State the blood parasite species.
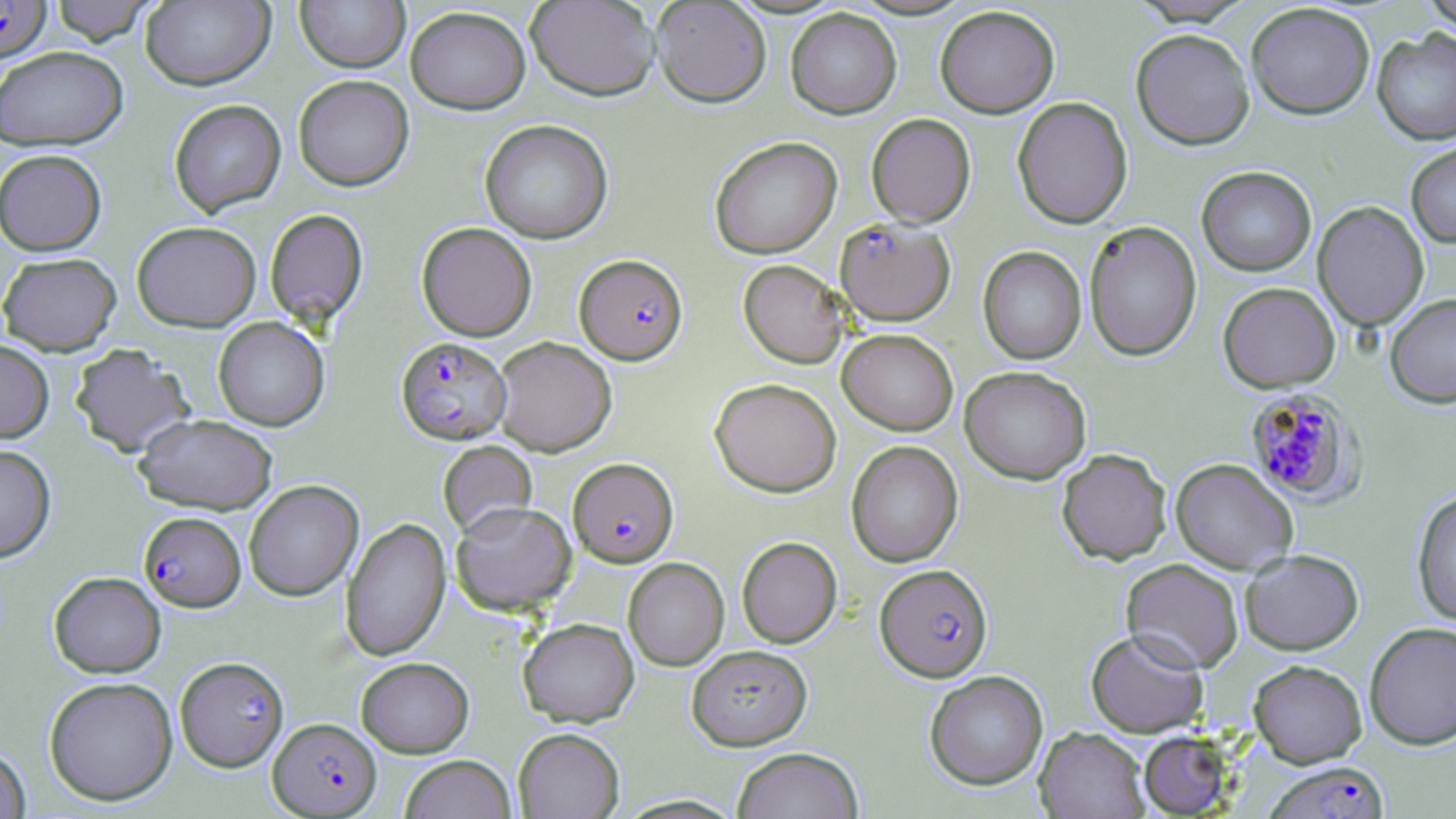
Plasmodium falciparum.

Approximate bounding boxes as (x1,y1)-(x2,y2) corner pairs in pixels. Uninfected red blood cell locations: (46,0)-(161,45), (295,0)-(410,73), (525,0)-(660,101), (1419,0)-(1456,35), (140,1)-(275,90), (651,1)-(771,107), (1245,2)-(1375,119), (405,5)-(530,114), (934,5)-(1059,118), (785,8)-(902,119), (1131,28)-(1255,150), (1372,29)-(1456,146), (0,46)-(128,151), (293,74)-(414,191), (1012,96)-(1133,228), (168,99)-(286,217), (866,113)-(976,228), (479,119)-(613,244), (709,136)-(842,259), (1406,141)-(1456,248), (0,149)-(107,255), (1197,166)-(1317,276), (1313,201)-(1429,332), (264,208)-(368,328), (1084,220)-(1202,361), (131,221)-(261,331), (416,222)-(537,341), (978,246)-(1086,364), (0,252)-(121,356), (738,259)-(849,368), (1218,282)-(1340,392), (1385,293)-(1456,409), (213,317)-(329,431), (837,328)-(958,435), (492,336)-(616,456), (0,340)-(54,443), (69,343)-(194,458), (960,365)-(1091,484), (710,378)-(842,497), (134,413)-(278,514), (438,440)-(537,537), (846,441)-(963,567), (0,444)-(56,563), (1057,448)-(1171,564), (1171,458)-(1297,574), (244,480)-(363,601), (1412,489)-(1456,627), (450,500)-(577,615), (341,517)-(451,661), (737,537)-(842,648), (1240,549)-(1363,655), (623,558)-(729,671), (1121,559)-(1243,673), (49,571)-(165,677), (518,618)-(639,726), (1364,622)-(1456,750), (1086,629)-(1208,737), (687,644)-(812,750), (356,656)-(473,757), (1248,659)-(1367,767), (925,670)-(1048,790), (43,676)-(178,805), (513,727)-(625,819), (1035,727)-(1150,818), (1139,731)-(1233,817), (0,744)-(31,818), (731,746)-(864,819), (399,755)-(517,819). Plasmodium falciparum-infected red blood cell locations: (0,0)-(51,62), (835,218)-(955,326), (574,254)-(687,365), (396,337)-(511,444), (1244,387)-(1365,504), (568,457)-(678,567), (139,511)-(245,612), (875,563)-(993,681), (177,660)-(290,775), (268,718)-(381,817), (1265,761)-(1389,819). 1000x magnification. One field of a larger specimen. Optical microscopy. May-Grünwald-Giemsa-stained preparation. Thin blood film. Image is 1456×819 pixels.